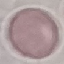 Malaria status: uninfected. Giemsa stain. Acquired by smartphone through the microscope eyepiece. Thin blood smear. Automatically extracted cell patch, resized to 64 × 64 pixels.